Assess this cell for malaria.
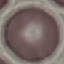

It is uninfected.

Acquired by smartphone through the microscope eyepiece. Thin smear of blood. Automatically extracted cell patch, resized to 64 × 64 pixels. Giemsa-stained preparation.